State which parasite is depicted.
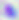

Toxoplasma gondii.

Summary:
  - Modality: micrograph
  - Magnification: 400x